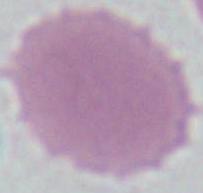
Summary:
  - Magnification: 1000x
  - Modality: micrograph
  - Identification: red blood cell